Locate every blood parasite and identify its species.
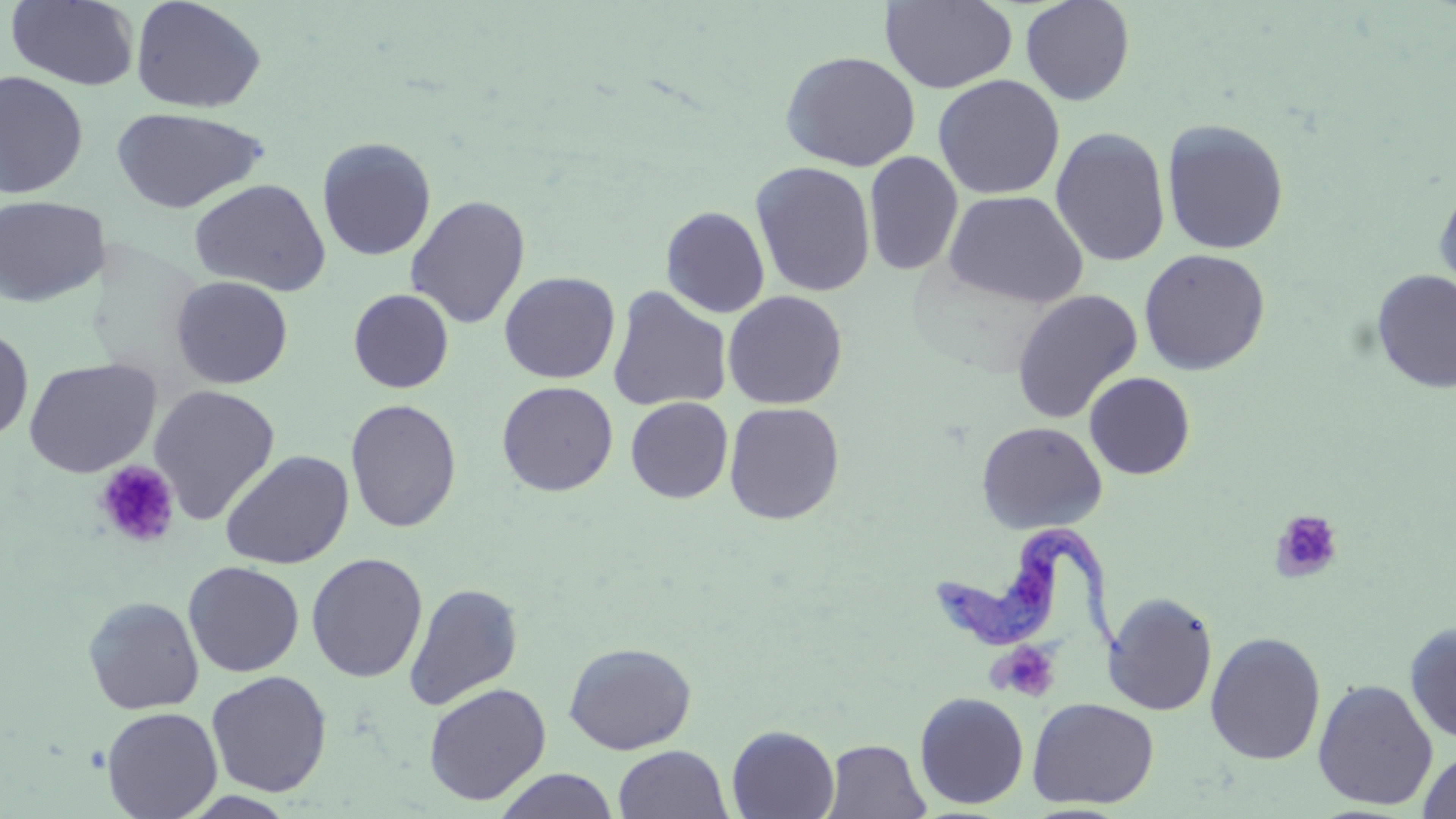

Approximate bounding boxes as named x1/y1/x2/y2 corners in pixels.
Trypanosoma brucei: (x1=924, y1=521, x2=1133, y2=664).
No Plasmodium falciparum, Plasmodium ovale, Plasmodium malariae, Plasmodium vivax, or Babesia divergens observed.

Summary:
  - Platelet locations: (x1=94, y1=460, x2=181, y2=548), (x1=1271, y1=510, x2=1344, y2=583), (x1=990, y1=641, x2=1059, y2=702)
  - Uninfected red blood cell locations: (x1=130, y1=0, x2=267, y2=114), (x1=1020, y1=0, x2=1135, y2=105), (x1=5, y1=1, x2=140, y2=91), (x1=879, y1=1, x2=1018, y2=93), (x1=781, y1=51, x2=921, y2=171), (x1=0, y1=70, x2=89, y2=199), (x1=933, y1=74, x2=1065, y2=200), (x1=110, y1=106, x2=268, y2=214), (x1=1162, y1=119, x2=1290, y2=255), (x1=1050, y1=127, x2=1170, y2=267), (x1=317, y1=136, x2=436, y2=261), (x1=864, y1=152, x2=963, y2=276), (x1=750, y1=162, x2=876, y2=298), (x1=189, y1=178, x2=331, y2=296), (x1=1433, y1=179, x2=1456, y2=307), (x1=943, y1=189, x2=1088, y2=308), (x1=0, y1=195, x2=109, y2=307), (x1=406, y1=195, x2=531, y2=329), (x1=661, y1=206, x2=770, y2=318), (x1=1138, y1=248, x2=1270, y2=375), (x1=1372, y1=270, x2=1456, y2=393), (x1=499, y1=271, x2=620, y2=383), (x1=170, y1=275, x2=294, y2=389), (x1=607, y1=287, x2=732, y2=412), (x1=348, y1=289, x2=454, y2=393), (x1=1011, y1=289, x2=1143, y2=424), (x1=722, y1=290, x2=847, y2=409), (x1=0, y1=326, x2=34, y2=443), (x1=23, y1=357, x2=161, y2=477), (x1=1084, y1=372, x2=1196, y2=480), (x1=497, y1=381, x2=618, y2=496), (x1=149, y1=385, x2=281, y2=524), (x1=625, y1=397, x2=733, y2=503), (x1=344, y1=398, x2=462, y2=533), (x1=724, y1=402, x2=846, y2=524), (x1=976, y1=421, x2=1107, y2=535), (x1=218, y1=449, x2=354, y2=569), (x1=305, y1=553, x2=428, y2=682), (x1=183, y1=561, x2=304, y2=677), (x1=403, y1=583, x2=524, y2=711), (x1=1103, y1=592, x2=1218, y2=716), (x1=82, y1=595, x2=205, y2=714), (x1=1404, y1=621, x2=1456, y2=744), (x1=1205, y1=631, x2=1326, y2=765), (x1=563, y1=641, x2=696, y2=755), (x1=206, y1=671, x2=332, y2=797), (x1=1313, y1=678, x2=1438, y2=810), (x1=422, y1=682, x2=551, y2=805), (x1=914, y1=691, x2=1029, y2=810), (x1=1027, y1=696, x2=1159, y2=809), (x1=101, y1=706, x2=223, y2=819), (x1=726, y1=724, x2=840, y2=819), (x1=821, y1=739, x2=930, y2=819), (x1=613, y1=745, x2=732, y2=818), (x1=1417, y1=748, x2=1456, y2=819), (x1=493, y1=768, x2=620, y2=819)
  - Slide-level diagnosis: Trypanosoma brucei
  - Preparation: thin blood film
  - Field of view: one of a larger specimen
  - Image size: 1456×819 pixels
  - Magnification: 1000x
  - Stain: May-Grünwald-Giemsa
  - Modality: light microscopy